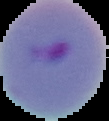
{
  "image_type": "segmented cell region on a black background",
  "result": "malaria parasites identified",
  "preparation": "thin blood film",
  "image_size": "109×121 pixels"
}